Describe the morphology of the erythrocytes.
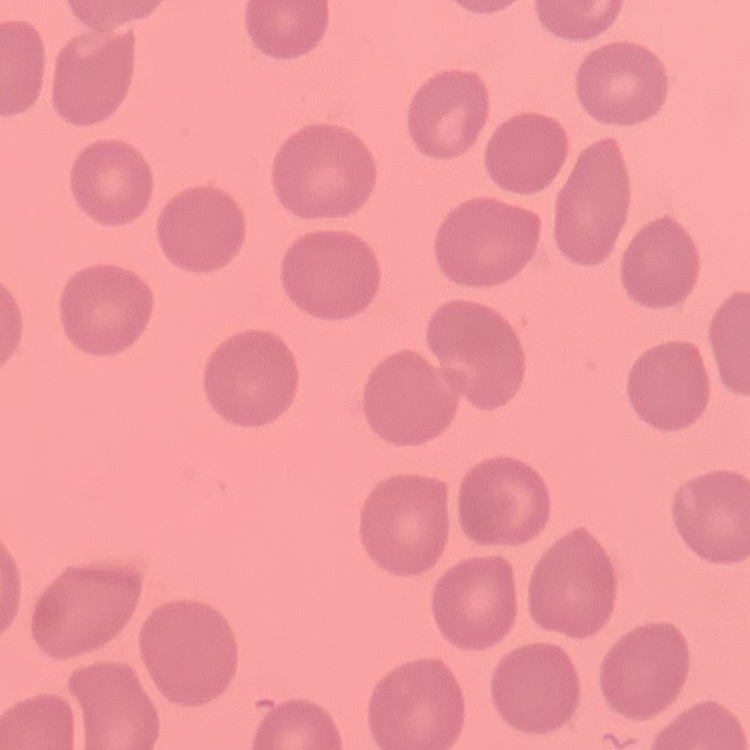
They show no rouleaux formation.

{
  "stain": "Field's or Giemsa",
  "preparation": "thin peripheral smear",
  "image_type": "one tile cut from a larger photomicrograph"
}